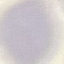

result = no malaria parasites seen
image type = automatically extracted cell patch, resized to 64 × 64 pixels
stain = Giemsa
capture = smartphone camera at the microscope eyepiece
preparation = thin blood film